Identify the preparation type.
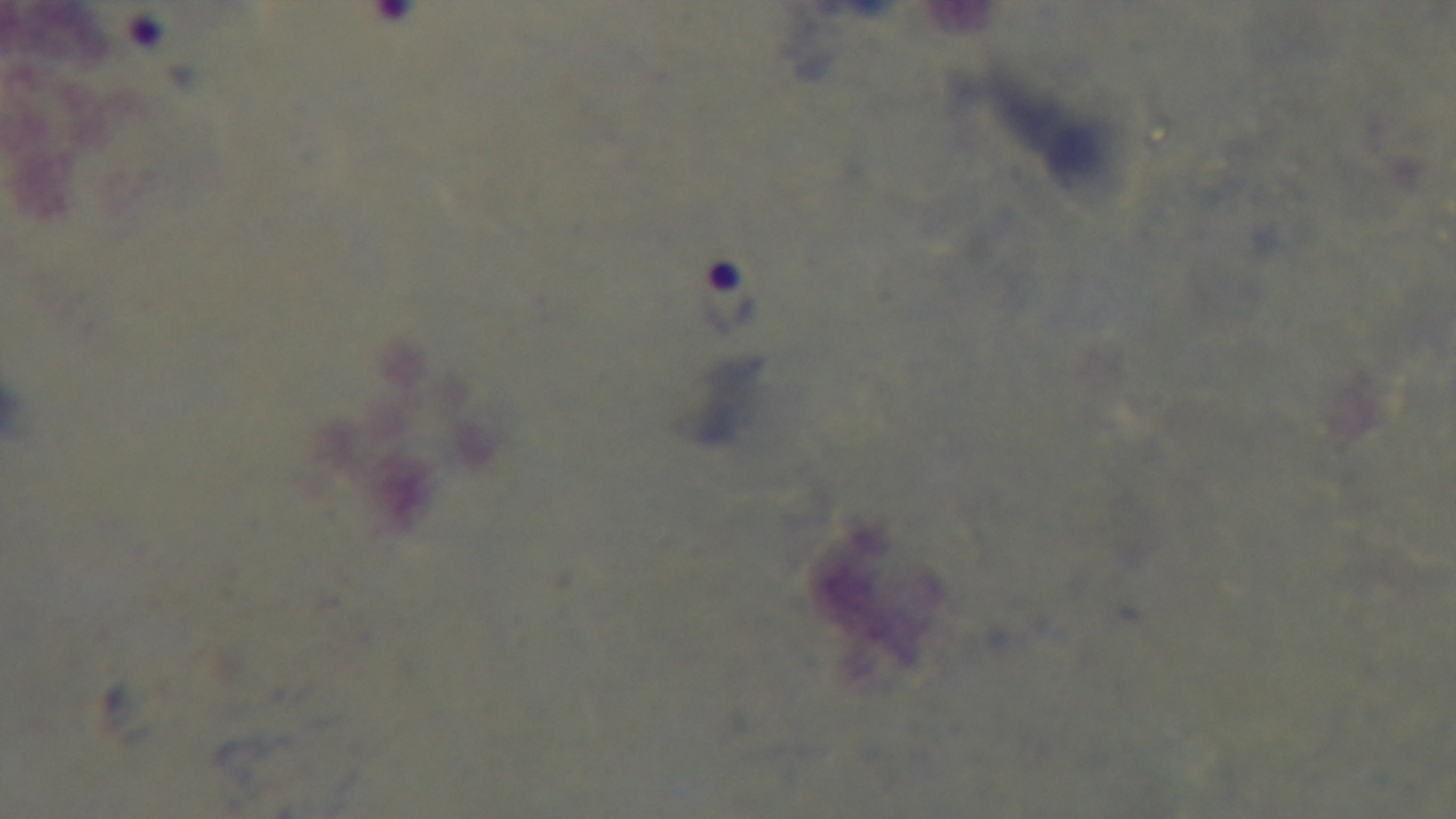
It is a thick blood film.

{
  "objective": "100x oil immersion",
  "field_of_view": "single",
  "capture": "mounted 4K digital camera",
  "malaria_status": "infected",
  "stain": "Giemsa",
  "modality": "light microscopy"
}